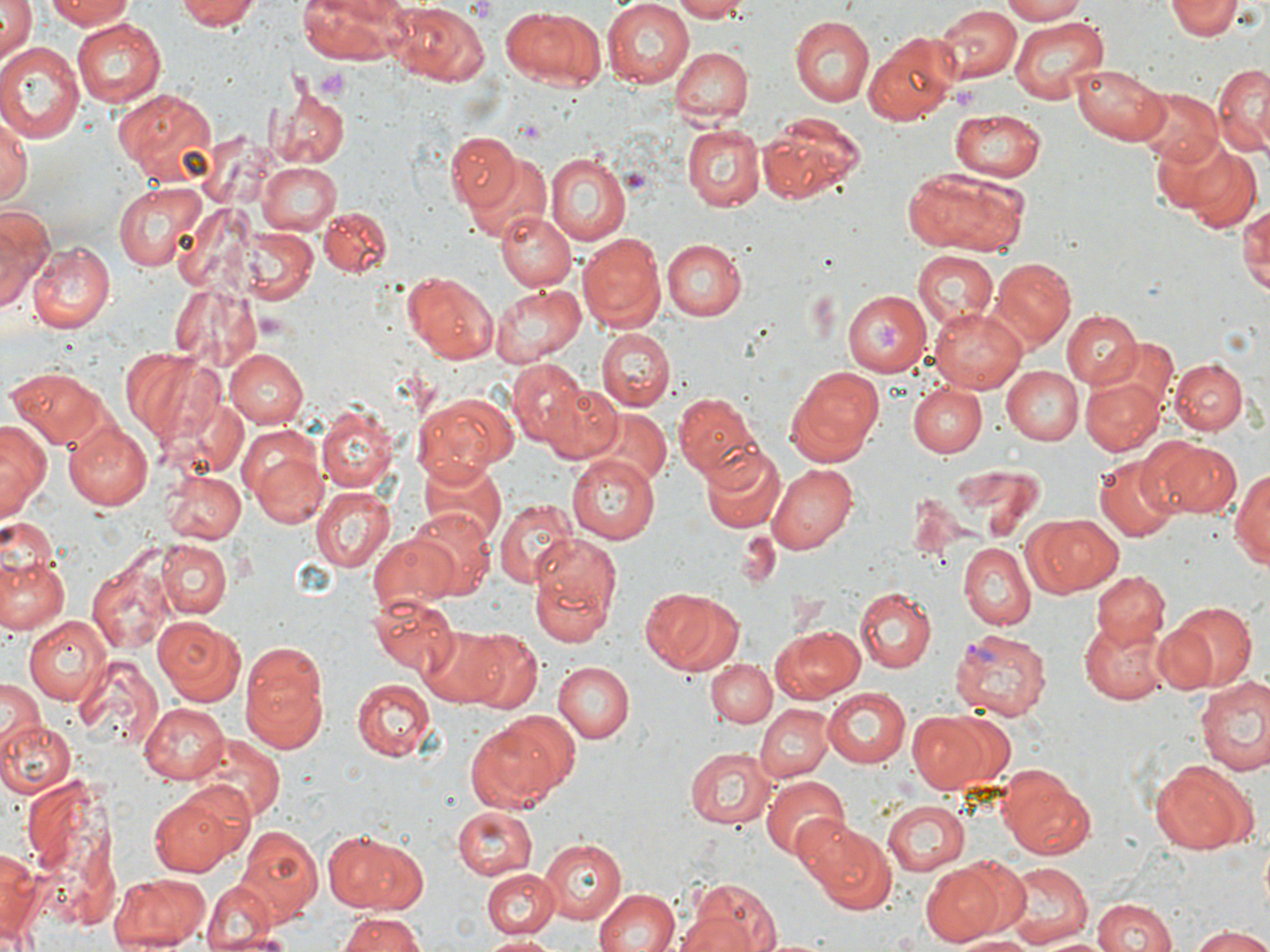
slide-level diagnosis = Plasmodium vivax
magnification = 1000x
modality = optical microscopy
preparation = thin blood film
image size = 1270×952 pixels
uninfected red blood cell locations = approximate bounding boxes as [x1, y1, x2, y2] in pixels: [43, 0, 139, 29], [173, 0, 262, 30], [298, 0, 408, 64], [602, 0, 694, 87], [673, 0, 748, 21], [997, 0, 1089, 24], [1166, 0, 1241, 40], [0, 1, 35, 70], [498, 3, 604, 91], [387, 4, 489, 87], [934, 5, 1020, 86], [1010, 16, 1106, 103], [72, 17, 166, 103], [789, 17, 875, 106], [866, 30, 962, 123], [0, 41, 84, 142], [669, 48, 750, 124], [1213, 58, 1268, 154], [1072, 61, 1170, 145], [270, 86, 349, 170], [115, 88, 218, 185], [1139, 88, 1221, 170], [679, 105, 759, 296], [948, 109, 1047, 181], [0, 112, 31, 210], [760, 112, 865, 204], [681, 122, 766, 212], [444, 132, 525, 214], [1162, 138, 1263, 231], [454, 150, 549, 245], [546, 152, 632, 245], [259, 162, 342, 234], [901, 165, 1029, 255], [113, 180, 206, 272], [1241, 199, 1270, 296], [319, 206, 393, 279], [0, 207, 52, 308], [496, 208, 576, 292], [239, 227, 319, 305], [577, 233, 665, 334], [661, 238, 746, 319], [26, 240, 115, 332], [913, 253, 998, 332], [991, 258, 1075, 348], [401, 272, 499, 362], [169, 282, 265, 374], [490, 282, 587, 368], [842, 291, 931, 377], [930, 304, 1028, 392], [1061, 310, 1143, 390], [597, 329, 674, 411], [224, 349, 307, 428], [120, 350, 223, 446], [1172, 359, 1248, 435], [506, 360, 588, 448], [1002, 364, 1082, 445], [787, 365, 885, 465], [6, 367, 109, 447], [1083, 377, 1162, 458], [537, 381, 624, 465], [907, 383, 986, 458], [26, 385, 143, 502], [414, 392, 516, 480], [677, 392, 761, 483], [585, 409, 670, 489], [315, 410, 399, 493], [0, 419, 49, 519], [65, 421, 156, 509], [242, 426, 327, 529], [1150, 438, 1242, 518], [699, 444, 784, 533], [566, 455, 658, 543], [1092, 455, 1181, 540], [420, 458, 505, 548], [947, 461, 1043, 542], [767, 463, 858, 553], [1232, 465, 1270, 574], [163, 470, 245, 545], [311, 487, 393, 572], [494, 496, 577, 588], [407, 506, 494, 598], [1022, 514, 1122, 599], [368, 530, 458, 612], [737, 530, 777, 591], [528, 534, 624, 639], [160, 542, 233, 620], [958, 543, 1033, 628], [0, 553, 69, 636], [89, 554, 174, 653], [1092, 571, 1169, 649], [641, 586, 736, 673], [854, 588, 937, 672], [369, 592, 460, 674], [1168, 601, 1259, 690], [155, 615, 247, 705], [24, 616, 111, 705], [1081, 618, 1173, 703], [1149, 621, 1218, 695], [770, 624, 866, 703], [417, 625, 512, 708], [459, 630, 542, 714], [239, 646, 329, 755], [73, 654, 163, 754], [706, 657, 776, 729], [554, 662, 634, 744], [1195, 675, 1270, 778], [353, 678, 433, 761], [0, 679, 44, 748], [821, 688, 911, 770], [138, 703, 231, 783], [757, 705, 831, 782], [908, 709, 1002, 794], [465, 715, 572, 811], [0, 719, 75, 797], [192, 736, 286, 820], [682, 745, 775, 830], [1149, 760, 1255, 854], [996, 763, 1098, 861], [21, 775, 124, 928], [759, 777, 849, 861], [150, 789, 241, 875], [881, 800, 971, 875], [451, 808, 538, 880], [802, 822, 895, 915], [235, 824, 323, 918], [322, 830, 427, 912], [539, 838, 625, 924], [0, 845, 41, 947], [950, 857, 1033, 939], [920, 862, 1003, 946], [995, 862, 1094, 945], [481, 869, 558, 940], [108, 872, 210, 951], [683, 878, 783, 952], [200, 881, 286, 949], [593, 888, 680, 952], [1090, 896, 1176, 952], [337, 911, 427, 952], [1186, 927, 1270, 952], [957, 933, 1039, 952], [477, 934, 562, 952]
field of view = one of a larger specimen
stain = May-Grünwald-Giemsa
platelet locations = approximate bounding boxes as [x1, y1, x2, y2] in pixels: [464, 0, 498, 22], [319, 69, 350, 101], [622, 168, 654, 198], [868, 321, 907, 353]
Plasmodium vivax-infected red blood cell locations = approximate bounding boxes as [x1, y1, x2, y2] in pixels: [949, 625, 1052, 720]